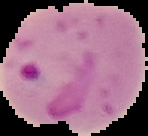
result = malaria parasites identified
image type = segmented cell region with the area outside set to black
image size = 148×136 pixels
preparation = thin blood smear